Outline platelets.
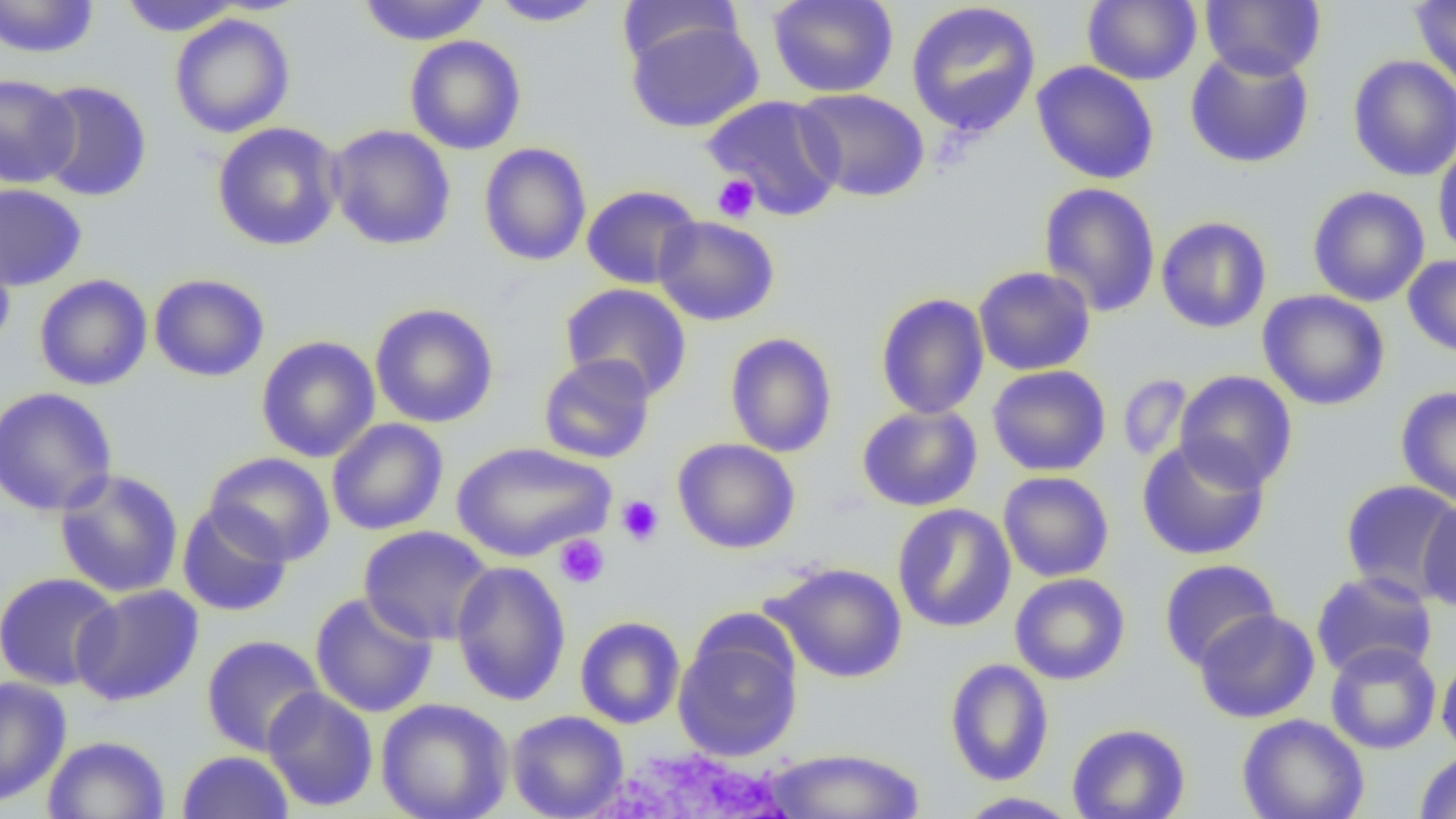

Approximate bounding boxes as (x1, y1, x2, y2) in pixels.
Platelets: (712, 174, 760, 223), (616, 495, 664, 547), (554, 534, 610, 589).

Summary:
  - Uninfected red blood cell locations: (0, 0, 100, 58), (117, 0, 243, 36), (356, 0, 491, 46), (488, 0, 606, 27), (767, 0, 899, 98), (1083, 0, 1201, 85), (1199, 0, 1326, 81), (1411, 0, 1456, 92), (616, 1, 744, 71), (905, 1, 1042, 138), (169, 14, 295, 138), (625, 18, 765, 133), (404, 35, 527, 155), (1184, 48, 1315, 169), (1347, 54, 1456, 182), (1031, 61, 1160, 184), (0, 73, 80, 189), (35, 79, 152, 202), (793, 87, 930, 202), (702, 94, 846, 221), (211, 121, 344, 251), (327, 124, 456, 250), (1432, 138, 1456, 261), (478, 142, 592, 267), (1038, 182, 1161, 318), (0, 183, 87, 291), (581, 184, 702, 289), (1307, 185, 1430, 307), (652, 215, 780, 326), (1155, 216, 1272, 333), (0, 236, 16, 354), (1403, 253, 1456, 358), (973, 266, 1096, 376), (149, 273, 270, 382), (34, 274, 153, 392), (560, 283, 692, 401), (1258, 290, 1390, 411), (875, 292, 990, 420), (369, 303, 500, 428), (724, 332, 838, 458), (256, 336, 380, 462), (538, 354, 656, 464), (987, 365, 1111, 476), (1174, 370, 1298, 493), (1117, 374, 1193, 463), (1395, 385, 1456, 508), (0, 387, 118, 517), (857, 404, 983, 512), (326, 418, 449, 536), (672, 437, 800, 554), (1137, 437, 1270, 561), (451, 441, 614, 562), (204, 451, 336, 566), (54, 469, 184, 598), (998, 471, 1114, 582), (1340, 480, 1456, 602), (1417, 496, 1456, 612), (177, 503, 293, 617), (893, 503, 1015, 633), (358, 525, 496, 646), (1158, 559, 1281, 670), (451, 560, 571, 706), (764, 562, 908, 684), (1310, 570, 1437, 680), (0, 572, 122, 691), (1009, 572, 1130, 685), (70, 585, 204, 707), (309, 592, 438, 718), (1193, 608, 1320, 723), (575, 616, 685, 729), (673, 621, 803, 762), (201, 634, 325, 756), (1325, 641, 1441, 754), (1436, 651, 1456, 760), (944, 658, 1054, 786), (0, 675, 72, 808), (262, 687, 379, 812), (376, 697, 513, 819), (506, 710, 629, 819), (1236, 713, 1369, 819), (1067, 723, 1191, 819), (42, 735, 170, 819), (761, 746, 927, 819), (177, 750, 294, 819), (1414, 750, 1456, 818), (955, 791, 1082, 818)
  - White blood cell locations: (578, 742, 800, 819)
  - Slide-level diagnosis: no evidence of blood parasites
  - Magnification: 1000x
  - Field of view: single
  - Modality: optical microscopy
  - Preparation: thin blood smear
  - Image size: 1456×819 pixels